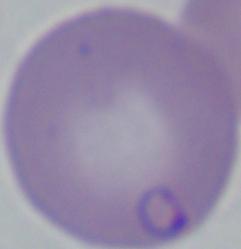

Photomicrograph. A Babesia parasite is shown. Captured at 1000x magnification.